Identify the blood parasite species.
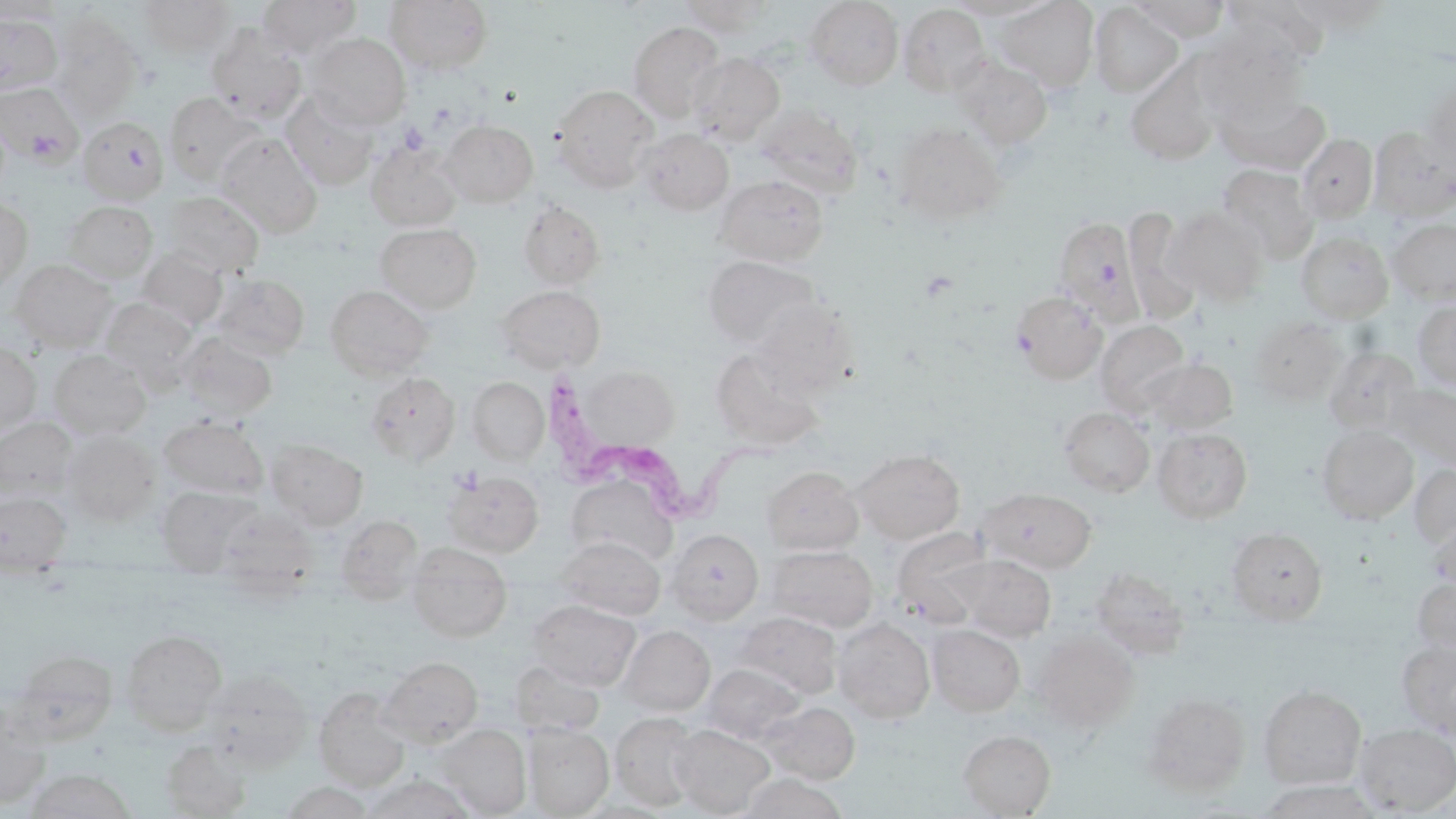
Trypanosoma brucei.

Approximate bounding boxes as (x1, y1, x2, y2) in pixels. Uninfected red blood cell locations: (138, 0, 234, 58), (257, 0, 361, 57), (385, 0, 493, 74), (944, 0, 1057, 20), (993, 0, 1100, 91), (1129, 0, 1230, 41), (0, 1, 63, 24), (676, 1, 777, 36), (804, 1, 904, 89), (1220, 1, 1330, 72), (1285, 1, 1392, 34), (1090, 3, 1184, 97), (898, 4, 990, 96), (0, 13, 61, 97), (51, 16, 143, 120), (628, 22, 725, 122), (205, 24, 307, 123), (1194, 29, 1305, 120), (304, 33, 411, 129), (687, 52, 784, 145), (952, 56, 1053, 150), (1126, 60, 1221, 167), (1422, 81, 1456, 172), (0, 82, 83, 166), (551, 84, 659, 192), (1216, 88, 1329, 174), (280, 91, 378, 190), (164, 92, 265, 186), (755, 104, 863, 198), (440, 119, 538, 207), (83, 122, 170, 206), (892, 122, 1007, 225), (1369, 126, 1456, 221), (637, 129, 733, 215), (216, 133, 322, 237), (1297, 134, 1378, 222), (366, 139, 463, 231), (1217, 163, 1319, 263), (714, 174, 830, 265), (163, 191, 264, 277), (0, 199, 32, 294), (517, 200, 605, 290), (64, 201, 157, 281), (1123, 207, 1200, 324), (1164, 207, 1271, 306), (1052, 216, 1141, 324), (1388, 218, 1456, 304), (375, 223, 481, 314), (1296, 231, 1393, 323), (138, 247, 227, 331), (702, 255, 820, 349), (11, 259, 115, 351), (211, 273, 310, 359), (325, 285, 434, 379), (496, 285, 605, 373), (1011, 290, 1109, 384), (750, 297, 857, 397), (100, 298, 197, 387), (1411, 299, 1456, 391), (1249, 317, 1346, 405), (1095, 320, 1190, 415), (178, 332, 277, 420), (0, 344, 41, 433), (1323, 345, 1421, 435), (711, 348, 827, 449), (49, 350, 150, 440), (1142, 357, 1238, 435), (570, 363, 682, 462), (366, 372, 459, 465), (468, 377, 549, 464), (1384, 381, 1456, 472), (1058, 407, 1154, 496), (159, 416, 268, 499), (0, 417, 76, 500), (1317, 425, 1419, 524), (1153, 427, 1253, 524), (62, 431, 160, 525), (266, 440, 367, 529), (853, 448, 965, 544), (1410, 464, 1456, 550), (762, 465, 863, 554), (444, 470, 544, 557), (565, 476, 675, 568), (156, 486, 259, 573), (979, 487, 1097, 573), (0, 492, 70, 572), (335, 515, 423, 601), (1427, 518, 1456, 590), (1226, 527, 1327, 623), (666, 528, 764, 624), (891, 528, 993, 626), (558, 536, 664, 620), (407, 545, 512, 641), (767, 545, 877, 632), (952, 555, 1056, 641), (1089, 564, 1191, 660), (1413, 577, 1456, 660), (529, 599, 640, 690), (735, 611, 841, 699), (833, 617, 935, 723), (928, 624, 1025, 716), (618, 625, 715, 716), (121, 629, 226, 733), (1031, 630, 1140, 731), (1397, 640, 1456, 737), (8, 650, 117, 744), (379, 656, 482, 746), (510, 662, 604, 737), (701, 663, 804, 745), (205, 669, 312, 771), (1258, 685, 1366, 790), (314, 686, 411, 790), (1142, 692, 1250, 796), (0, 699, 52, 808), (762, 701, 860, 784), (611, 713, 700, 811), (670, 724, 775, 817), (1353, 724, 1455, 814), (437, 725, 530, 817), (524, 725, 614, 816), (958, 729, 1055, 817), (161, 739, 251, 817), (23, 768, 137, 818), (364, 773, 476, 818), (738, 773, 846, 819), (279, 782, 375, 818). Platelet locations: (399, 121, 430, 155). Trypanosoma brucei locations: (546, 368, 786, 519). Image is 1456×819 pixels. Captured at 1000x magnification. May-Grünwald-Giemsa-stained preparation. Thin blood film. Light microscopy. Single field of view.